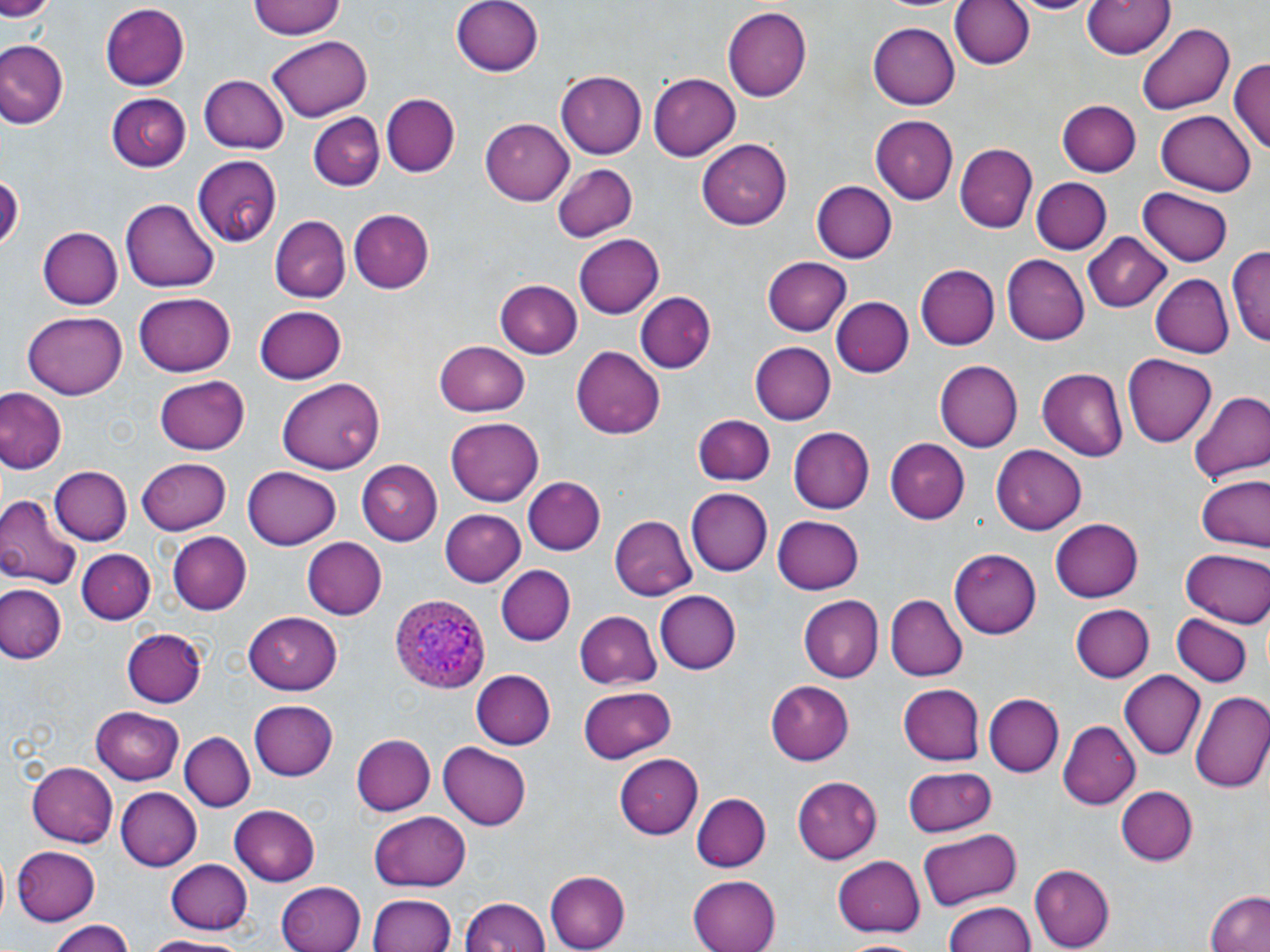
slide-level diagnosis = Plasmodium ovale
uninfected red blood cell locations = approximate bounding boxes as (x1, y1, x2, y2) in pixels: (248, 0, 347, 41), (452, 0, 546, 75), (949, 0, 1034, 72), (1011, 0, 1096, 16), (1083, 0, 1175, 61), (0, 1, 54, 22), (98, 4, 193, 89), (1091, 5, 1220, 88), (722, 7, 811, 102), (867, 21, 960, 109), (1136, 23, 1234, 114), (266, 36, 373, 119), (0, 40, 67, 130), (1231, 58, 1270, 159), (199, 72, 292, 154), (555, 72, 648, 159), (647, 73, 740, 162), (106, 93, 191, 172), (382, 94, 460, 177), (1058, 99, 1140, 177), (1155, 110, 1257, 195), (309, 111, 383, 191), (868, 115, 956, 203), (482, 117, 573, 204), (697, 138, 794, 228), (955, 144, 1037, 232), (195, 154, 282, 245), (550, 161, 639, 242), (1, 175, 22, 251), (1030, 178, 1111, 255), (809, 179, 897, 267), (1137, 188, 1233, 266), (122, 197, 219, 293), (347, 209, 433, 293), (269, 216, 350, 303), (38, 226, 122, 309), (575, 232, 664, 319), (1084, 233, 1173, 312), (1230, 247, 1270, 351), (1002, 255, 1089, 344), (762, 258, 850, 337), (915, 264, 999, 350), (1151, 274, 1232, 359), (493, 277, 584, 360), (135, 289, 235, 375), (634, 291, 714, 371), (832, 297, 914, 377), (254, 305, 348, 384), (23, 310, 127, 399), (434, 340, 531, 417), (749, 342, 836, 423), (574, 345, 664, 438), (1121, 354, 1217, 449), (934, 359, 1022, 453), (1037, 368, 1129, 460), (154, 375, 249, 454), (276, 376, 382, 471), (0, 388, 66, 476), (1190, 391, 1269, 489), (693, 414, 775, 486), (446, 417, 544, 507), (788, 426, 874, 514), (885, 439, 970, 524), (991, 445, 1086, 535), (137, 456, 233, 532), (361, 460, 442, 546), (47, 465, 130, 545), (242, 466, 342, 550), (1193, 473, 1269, 554), (521, 476, 606, 555), (686, 488, 771, 576), (0, 494, 81, 591), (440, 509, 526, 586), (772, 512, 864, 593), (609, 515, 699, 600), (1052, 516, 1145, 603), (167, 532, 251, 614), (301, 538, 387, 618), (78, 547, 155, 623), (949, 548, 1040, 639), (1180, 548, 1270, 627), (494, 566, 578, 648), (0, 581, 67, 665), (655, 590, 741, 674), (886, 596, 967, 681), (799, 597, 882, 682), (1072, 605, 1153, 682), (245, 611, 344, 693), (574, 611, 662, 689), (1173, 616, 1251, 687), (122, 628, 207, 707), (471, 670, 556, 749), (1120, 671, 1205, 760), (767, 680, 854, 766), (897, 684, 985, 766), (577, 687, 674, 762), (1192, 689, 1270, 795), (985, 695, 1064, 776), (248, 699, 338, 781), (90, 705, 184, 783), (1058, 721, 1140, 808), (180, 731, 255, 811), (350, 734, 434, 817), (438, 742, 531, 830), (615, 754, 703, 838), (25, 762, 118, 847), (903, 767, 996, 835), (793, 775, 880, 864), (1116, 786, 1198, 866), (116, 788, 201, 870), (692, 793, 770, 872), (230, 805, 321, 887), (371, 811, 470, 890), (918, 828, 1023, 908), (10, 845, 102, 925), (834, 854, 925, 936), (167, 859, 252, 935), (1030, 865, 1114, 951), (542, 870, 628, 952), (688, 874, 780, 952), (276, 880, 366, 952), (1203, 888, 1270, 952), (370, 894, 454, 952), (462, 897, 549, 952), (943, 900, 1038, 952), (46, 919, 133, 952), (144, 934, 253, 951)
field of view = one of a larger specimen
modality = optical microscopy
Plasmodium ovale-infected red blood cell locations = approximate bounding boxes as (x1, y1, x2, y2) in pixels: (389, 593, 490, 696)
image size = 1270×952 pixels
preparation = thin blood smear
magnification = 1000x
stain = May-Grünwald-Giemsa